Locate every blood parasite and identify its species.
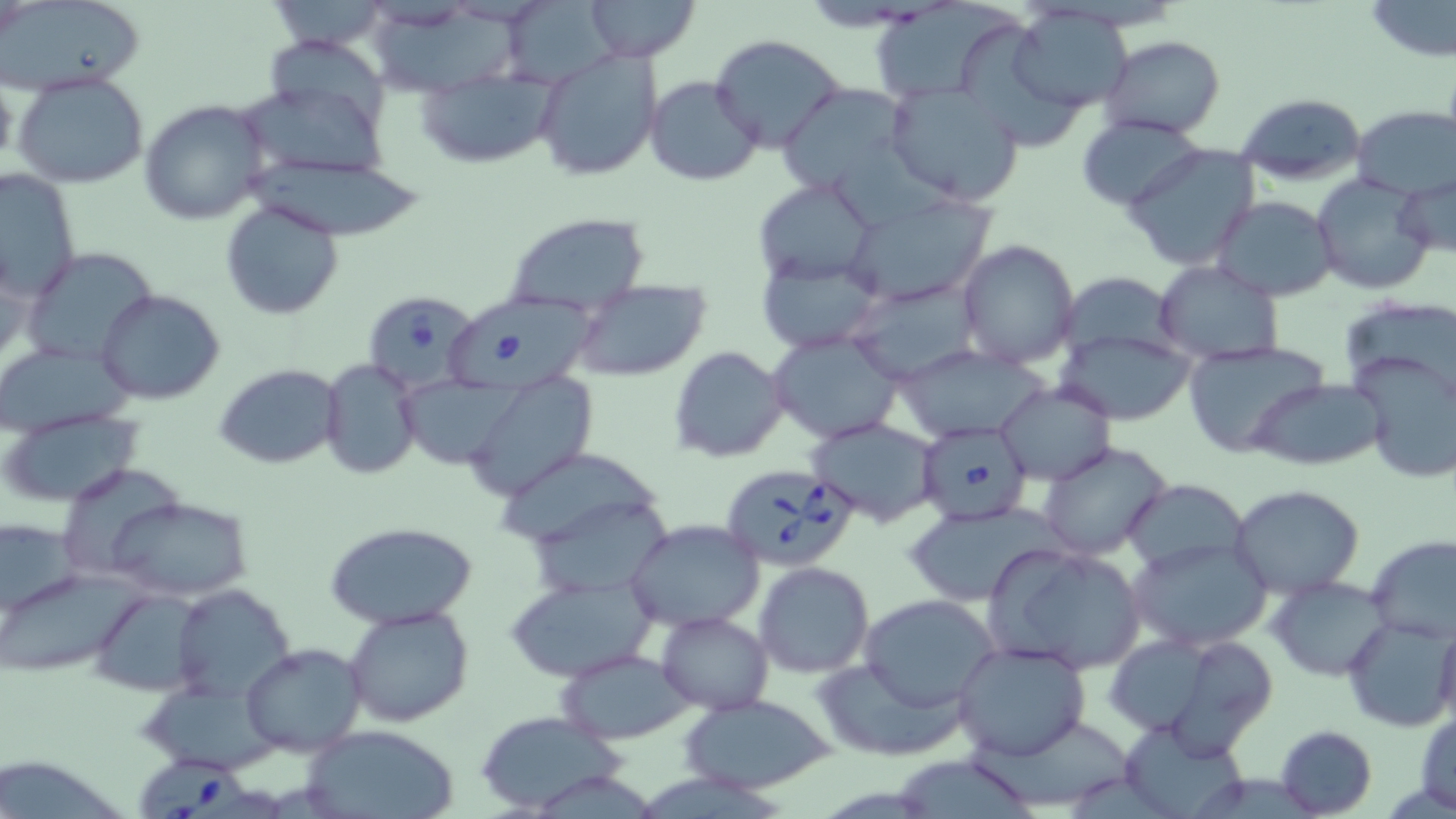
Approximate bounding boxes as named x1/y1/x2/y2 corners in pixels.
Babesia divergens-infected red blood cells: (x1=363, y1=291, x2=481, y2=390), (x1=442, y1=291, x2=600, y2=394), (x1=914, y1=421, x2=1035, y2=526), (x1=719, y1=463, x2=858, y2=571), (x1=140, y1=756, x2=253, y2=819).
No Plasmodium falciparum, Plasmodium ovale, Plasmodium malariae, Plasmodium vivax, or Trypanosoma brucei observed.

slide-level diagnosis = Babesia divergens
preparation = thin blood film
magnification = 1000x
stain = May-Grünwald-Giemsa
uninfected red blood cell locations = approximate bounding boxes as named x1/y1/x2/y2 corners in pixels: (x1=582, y1=0, x2=700, y2=62), (x1=867, y1=0, x2=1028, y2=105), (x1=1363, y1=0, x2=1455, y2=63), (x1=5, y1=1, x2=148, y2=95), (x1=508, y1=1, x2=633, y2=87), (x1=1011, y1=6, x2=1135, y2=113), (x1=372, y1=8, x2=535, y2=93), (x1=710, y1=34, x2=846, y2=154), (x1=1099, y1=34, x2=1225, y2=139), (x1=268, y1=40, x2=394, y2=143), (x1=533, y1=51, x2=663, y2=181), (x1=413, y1=71, x2=560, y2=167), (x1=12, y1=72, x2=150, y2=190), (x1=646, y1=76, x2=762, y2=186), (x1=885, y1=82, x2=1025, y2=205), (x1=776, y1=83, x2=913, y2=197), (x1=240, y1=91, x2=392, y2=184), (x1=1234, y1=92, x2=1365, y2=186), (x1=139, y1=99, x2=270, y2=224), (x1=1351, y1=107, x2=1456, y2=199), (x1=1077, y1=115, x2=1206, y2=211), (x1=1123, y1=144, x2=1258, y2=270), (x1=237, y1=154, x2=427, y2=239), (x1=0, y1=169, x2=81, y2=304), (x1=1312, y1=175, x2=1434, y2=295), (x1=752, y1=177, x2=877, y2=289), (x1=1395, y1=177, x2=1455, y2=259), (x1=842, y1=194, x2=999, y2=306), (x1=1211, y1=196, x2=1337, y2=302), (x1=219, y1=200, x2=344, y2=320), (x1=501, y1=213, x2=650, y2=314), (x1=956, y1=239, x2=1081, y2=369), (x1=23, y1=247, x2=162, y2=369), (x1=758, y1=255, x2=886, y2=353), (x1=1154, y1=259, x2=1283, y2=365), (x1=847, y1=278, x2=985, y2=384), (x1=571, y1=279, x2=711, y2=382), (x1=97, y1=288, x2=224, y2=405), (x1=1055, y1=330, x2=1195, y2=426), (x1=769, y1=331, x2=903, y2=444), (x1=1181, y1=340, x2=1332, y2=459), (x1=0, y1=343, x2=133, y2=434), (x1=894, y1=344, x2=1053, y2=441), (x1=669, y1=346, x2=788, y2=463), (x1=1350, y1=352, x2=1456, y2=485), (x1=321, y1=360, x2=420, y2=479), (x1=213, y1=362, x2=344, y2=470), (x1=465, y1=372, x2=599, y2=501), (x1=393, y1=374, x2=526, y2=470), (x1=1250, y1=379, x2=1387, y2=469), (x1=994, y1=382, x2=1115, y2=484), (x1=0, y1=409, x2=146, y2=508), (x1=805, y1=417, x2=942, y2=528), (x1=1037, y1=440, x2=1174, y2=562), (x1=502, y1=451, x2=668, y2=554), (x1=63, y1=469, x2=187, y2=573), (x1=1124, y1=478, x2=1251, y2=576), (x1=1229, y1=485, x2=1366, y2=598), (x1=99, y1=495, x2=255, y2=601), (x1=535, y1=503, x2=680, y2=595), (x1=903, y1=507, x2=1061, y2=607), (x1=2, y1=517, x2=81, y2=621), (x1=624, y1=518, x2=764, y2=632), (x1=324, y1=520, x2=480, y2=629), (x1=1366, y1=537, x2=1456, y2=641), (x1=1126, y1=538, x2=1275, y2=654), (x1=984, y1=543, x2=1150, y2=676), (x1=754, y1=561, x2=873, y2=678), (x1=1, y1=573, x2=155, y2=675), (x1=1268, y1=577, x2=1393, y2=679), (x1=502, y1=578, x2=658, y2=682), (x1=173, y1=582, x2=295, y2=704), (x1=99, y1=591, x2=229, y2=695), (x1=861, y1=594, x2=1002, y2=709), (x1=343, y1=606, x2=477, y2=728), (x1=655, y1=611, x2=772, y2=714), (x1=1344, y1=616, x2=1456, y2=733), (x1=1434, y1=621, x2=1456, y2=736), (x1=1106, y1=634, x2=1213, y2=735), (x1=952, y1=639, x2=1093, y2=760), (x1=241, y1=641, x2=368, y2=755), (x1=554, y1=648, x2=698, y2=744), (x1=813, y1=649, x2=977, y2=764), (x1=677, y1=695, x2=840, y2=792), (x1=1414, y1=707, x2=1456, y2=813), (x1=473, y1=710, x2=628, y2=814), (x1=1118, y1=718, x2=1249, y2=818), (x1=1274, y1=725, x2=1377, y2=817), (x1=300, y1=726, x2=463, y2=819)
image size = 1456×819 pixels
field of view = single
modality = light microscopy